Report the malaria status of this cell.
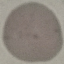

Uninfected.

image type = cell patch, automatically extracted from a larger field of view and resized to 64 × 64 pixels
stain = Giemsa
capture = smartphone through the microscope eyepiece
preparation = thin smear